State which parasite is depicted.
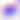

This is Toxoplasma gondii.

400x magnification. Micrograph.